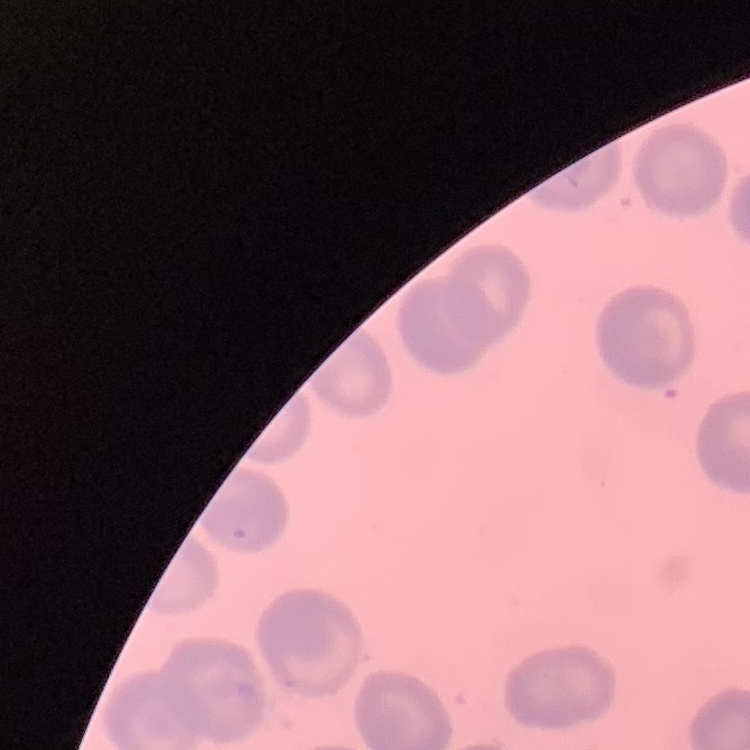 The red blood cells exhibit no rouleaux formation. One tile cut from a larger photomicrograph. Stained with either Field's or Giemsa. Thin peripheral smear.